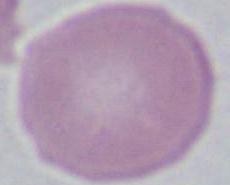
Summary:
  - Identification: erythrocyte
  - Modality: photomicrograph
  - Magnification: 1000x